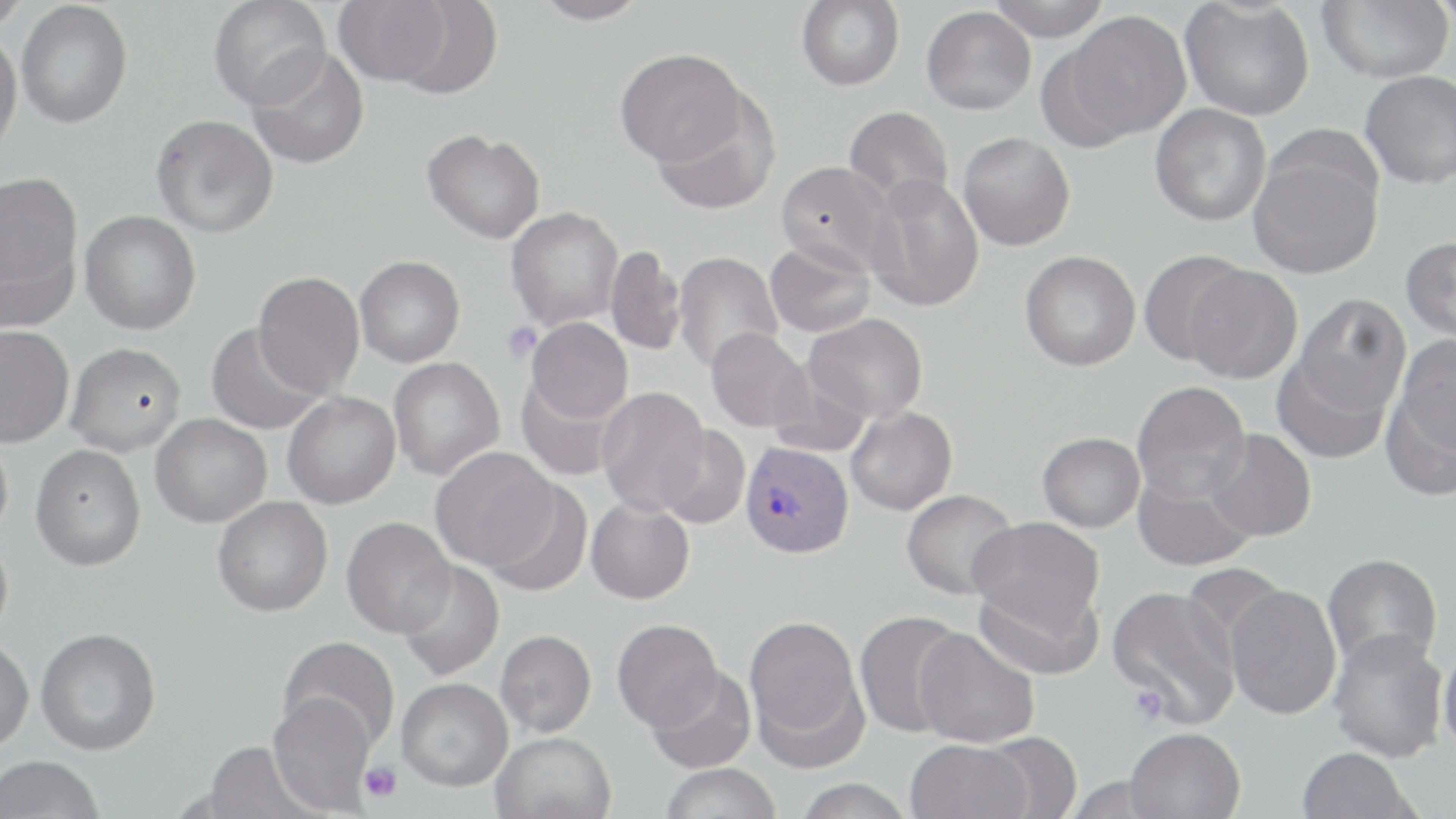
Plasmodium vivax-infected red blood cell locations = approximate bounding boxes as named x1/y1/x2/y2 corners in pixels: (x1=740, y1=441, x2=854, y2=558)
slide-level diagnosis = Plasmodium vivax
image size = 1456×819 pixels
uninfected red blood cell locations = approximate bounding boxes as named x1/y1/x2/y2 corners in pixels: (x1=0, y1=0, x2=30, y2=33), (x1=208, y1=0, x2=330, y2=110), (x1=532, y1=0, x2=650, y2=25), (x1=797, y1=0, x2=904, y2=90), (x1=986, y1=0, x2=1112, y2=41), (x1=1180, y1=0, x2=1314, y2=120), (x1=1317, y1=0, x2=1452, y2=83), (x1=334, y1=1, x2=451, y2=86), (x1=1428, y1=1, x2=1456, y2=29), (x1=16, y1=2, x2=132, y2=128), (x1=391, y1=2, x2=504, y2=99), (x1=921, y1=6, x2=1036, y2=114), (x1=1063, y1=11, x2=1192, y2=140), (x1=0, y1=31, x2=22, y2=162), (x1=247, y1=47, x2=369, y2=169), (x1=615, y1=48, x2=746, y2=168), (x1=1361, y1=70, x2=1456, y2=189), (x1=653, y1=90, x2=780, y2=214), (x1=1150, y1=103, x2=1272, y2=227), (x1=844, y1=106, x2=953, y2=210), (x1=151, y1=114, x2=278, y2=238), (x1=422, y1=129, x2=545, y2=244), (x1=958, y1=132, x2=1075, y2=251), (x1=1248, y1=145, x2=1383, y2=279), (x1=776, y1=161, x2=894, y2=275), (x1=0, y1=171, x2=82, y2=301), (x1=864, y1=173, x2=984, y2=312), (x1=506, y1=207, x2=623, y2=331), (x1=80, y1=210, x2=201, y2=334), (x1=1400, y1=236, x2=1456, y2=344), (x1=765, y1=240, x2=876, y2=337), (x1=605, y1=245, x2=687, y2=356), (x1=1139, y1=249, x2=1249, y2=365), (x1=1020, y1=250, x2=1141, y2=371), (x1=673, y1=252, x2=783, y2=374), (x1=354, y1=255, x2=465, y2=367), (x1=1184, y1=264, x2=1303, y2=384), (x1=253, y1=272, x2=364, y2=397), (x1=1294, y1=294, x2=1411, y2=416), (x1=804, y1=313, x2=928, y2=422), (x1=526, y1=316, x2=633, y2=423), (x1=206, y1=322, x2=325, y2=435), (x1=0, y1=324, x2=74, y2=447), (x1=706, y1=327, x2=811, y2=433), (x1=1394, y1=334, x2=1456, y2=458), (x1=65, y1=342, x2=186, y2=455), (x1=1272, y1=354, x2=1391, y2=464), (x1=388, y1=357, x2=505, y2=481), (x1=768, y1=360, x2=873, y2=458), (x1=516, y1=374, x2=623, y2=481), (x1=1381, y1=374, x2=1456, y2=502), (x1=1132, y1=381, x2=1250, y2=503), (x1=597, y1=387, x2=710, y2=516), (x1=282, y1=392, x2=400, y2=509), (x1=846, y1=406, x2=958, y2=515), (x1=151, y1=414, x2=271, y2=527), (x1=657, y1=425, x2=751, y2=528), (x1=1204, y1=428, x2=1317, y2=542), (x1=0, y1=429, x2=13, y2=545), (x1=1037, y1=432, x2=1145, y2=532), (x1=31, y1=444, x2=146, y2=570), (x1=430, y1=447, x2=558, y2=571), (x1=1133, y1=466, x2=1256, y2=571), (x1=482, y1=479, x2=593, y2=596), (x1=901, y1=489, x2=1019, y2=600), (x1=212, y1=497, x2=333, y2=616), (x1=586, y1=499, x2=694, y2=604), (x1=341, y1=516, x2=456, y2=638), (x1=969, y1=517, x2=1105, y2=637), (x1=0, y1=532, x2=13, y2=645), (x1=1322, y1=553, x2=1442, y2=673), (x1=396, y1=560, x2=505, y2=680), (x1=1180, y1=563, x2=1285, y2=667), (x1=973, y1=576, x2=1103, y2=680), (x1=1106, y1=585, x2=1241, y2=728), (x1=1225, y1=585, x2=1342, y2=720), (x1=854, y1=610, x2=969, y2=738), (x1=744, y1=614, x2=866, y2=762), (x1=612, y1=619, x2=723, y2=731), (x1=36, y1=627, x2=161, y2=754), (x1=914, y1=627, x2=1040, y2=748), (x1=495, y1=630, x2=597, y2=737), (x1=1329, y1=630, x2=1448, y2=762), (x1=278, y1=636, x2=400, y2=752), (x1=0, y1=637, x2=34, y2=753), (x1=1438, y1=641, x2=1456, y2=756), (x1=645, y1=666, x2=757, y2=773), (x1=396, y1=677, x2=513, y2=791), (x1=268, y1=692, x2=377, y2=815), (x1=1124, y1=727, x2=1246, y2=818), (x1=980, y1=730, x2=1083, y2=818), (x1=491, y1=731, x2=616, y2=819), (x1=905, y1=739, x2=1032, y2=819), (x1=201, y1=741, x2=320, y2=819), (x1=1297, y1=747, x2=1417, y2=819), (x1=1, y1=755, x2=105, y2=819), (x1=660, y1=763, x2=782, y2=818), (x1=793, y1=778, x2=913, y2=819)
platelet locations = approximate bounding boxes as named x1/y1/x2/y2 corners in pixels: (x1=503, y1=322, x2=542, y2=363), (x1=1129, y1=684, x2=1168, y2=724), (x1=360, y1=762, x2=401, y2=802)
magnification = 1000x
stain = May-Grünwald-Giemsa
field of view = one of a larger specimen
preparation = thin blood film
modality = light microscopy